Comment on the morphology of the red blood cells.
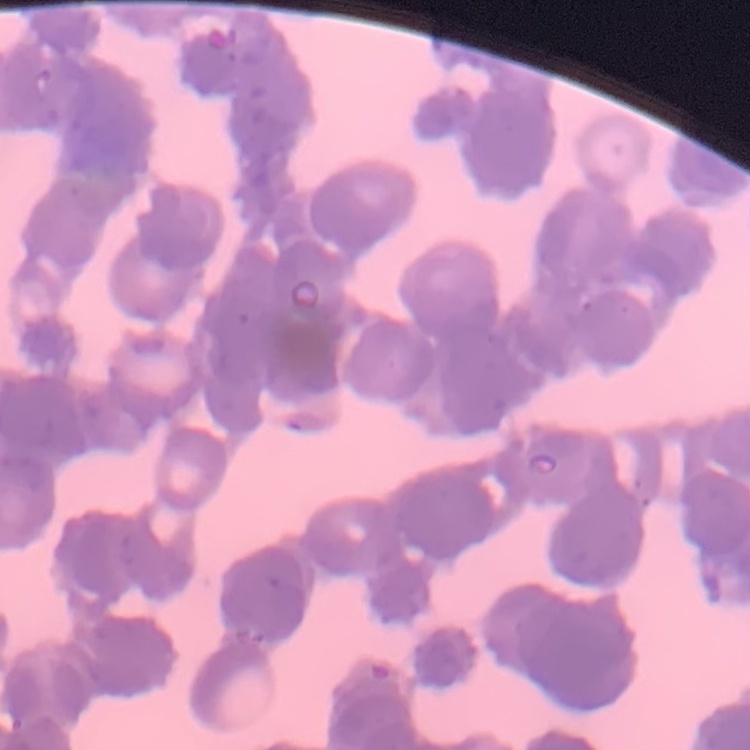
Rouleaux formation.

stain = Field's or Giemsa
preparation = thin peripheral smear
image type = square crop of a larger photomicrograph